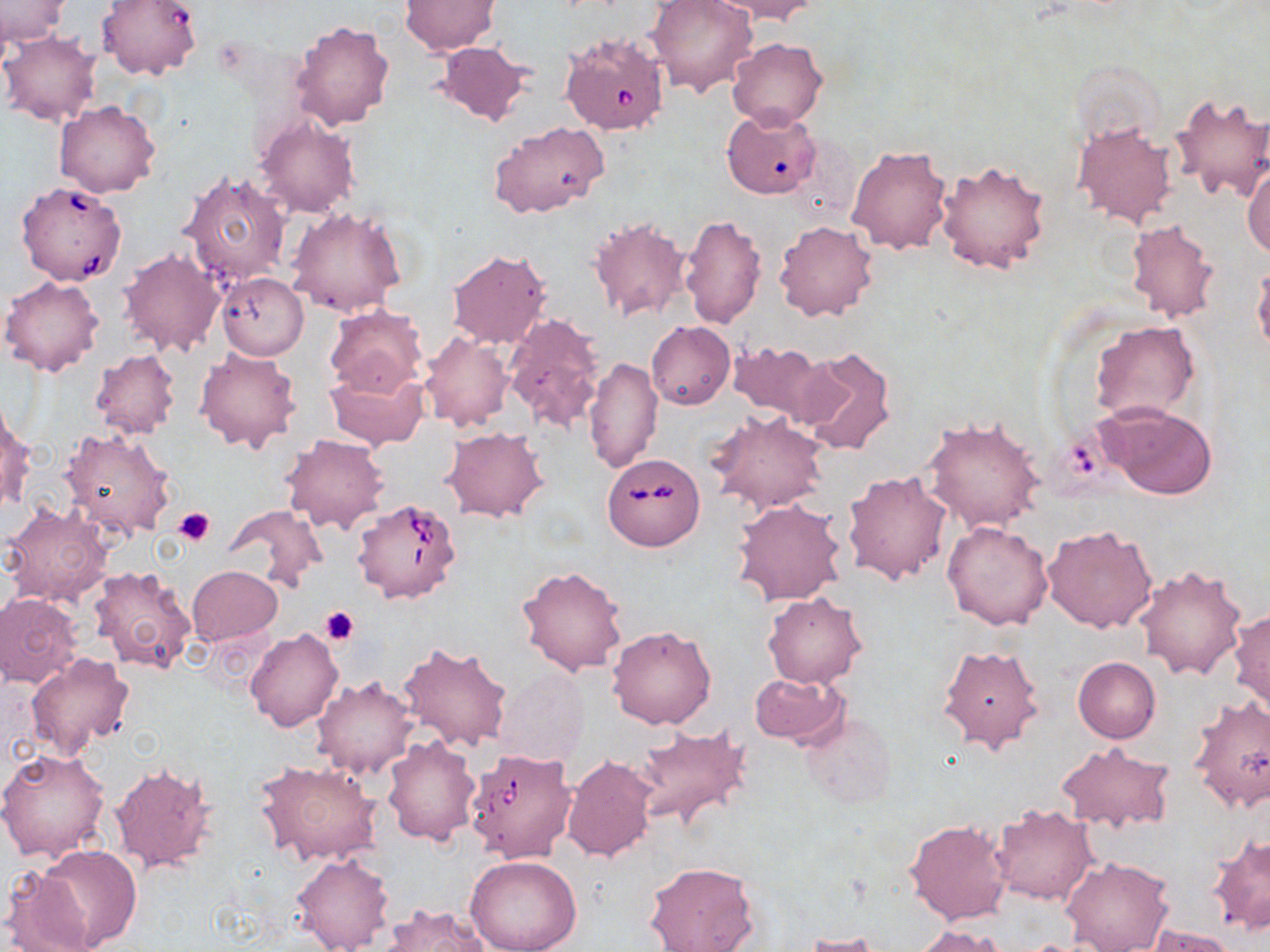

{
  "slide_level_diagnosis": "Babesia divergens",
  "field_of_view": "one of a larger specimen",
  "modality": "light microscopy",
  "magnification": "1000x",
  "stain": "May-Grünwald-Giemsa",
  "platelet_locations": "approximate bounding boxes as (x1, y1, x2, y2) in pixels: (172, 507, 215, 546), (320, 607, 359, 645)",
  "preparation": "thin blood smear",
  "image_size": "1270×952 pixels",
  "babesia_divergens_infected_red_blood_cell_locations": "approximate bounding boxes as (x1, y1, x2, y2) in pixels: (560, 32, 670, 136), (15, 180, 128, 286), (603, 451, 704, 551), (351, 497, 462, 603), (465, 749, 578, 862)",
  "uninfected_red_blood_cell_locations": "approximate bounding boxes as (x1, y1, x2, y2) in pixels: (1, 0, 68, 46), (98, 0, 202, 80), (646, 0, 759, 97), (713, 0, 820, 23), (2, 1, 83, 87), (399, 1, 500, 55), (290, 19, 394, 129), (0, 31, 101, 125), (727, 37, 826, 129), (431, 39, 532, 126), (1170, 92, 1270, 204), (56, 101, 160, 198), (723, 108, 821, 199), (253, 113, 362, 218), (488, 120, 609, 220), (1072, 122, 1178, 229), (847, 145, 951, 254), (936, 158, 1049, 275), (1244, 163, 1270, 260), (179, 169, 291, 289), (286, 206, 405, 318), (680, 214, 765, 331), (588, 216, 691, 323), (1125, 219, 1220, 324), (774, 220, 878, 322), (118, 246, 226, 357), (446, 249, 552, 348), (1252, 262, 1270, 358), (217, 273, 308, 359), (1, 276, 104, 377), (324, 306, 427, 398), (503, 313, 605, 436), (646, 320, 735, 409), (1090, 322, 1199, 424), (419, 331, 514, 432), (726, 339, 831, 425), (89, 348, 182, 439), (195, 348, 303, 453), (797, 348, 898, 456), (584, 358, 662, 472), (324, 368, 428, 452), (1095, 401, 1216, 500), (1, 405, 32, 517), (707, 411, 827, 513), (921, 417, 1046, 534), (441, 427, 549, 522), (60, 428, 176, 540), (281, 433, 390, 534), (842, 471, 952, 586), (732, 498, 846, 606), (2, 503, 113, 605), (224, 504, 326, 594), (942, 519, 1053, 630), (1042, 524, 1158, 633), (1134, 564, 1247, 682), (88, 565, 197, 673), (187, 565, 282, 646), (516, 565, 628, 677), (763, 592, 866, 688), (0, 593, 83, 687), (1230, 607, 1270, 717), (607, 625, 717, 730), (246, 627, 342, 731), (397, 639, 512, 751), (937, 642, 1045, 753), (27, 653, 135, 761), (1072, 657, 1160, 744), (496, 671, 589, 765), (749, 671, 849, 748), (312, 676, 420, 779), (761, 678, 884, 796), (1187, 694, 1270, 812), (799, 708, 898, 808), (633, 722, 752, 832), (382, 734, 481, 844), (1055, 741, 1176, 833), (0, 746, 110, 862), (561, 755, 657, 861), (255, 759, 382, 865), (108, 763, 219, 877), (990, 804, 1096, 904), (904, 819, 1011, 925), (1208, 833, 1270, 935), (32, 845, 142, 950), (291, 852, 394, 952), (466, 854, 583, 952), (1060, 855, 1175, 952), (644, 861, 758, 951), (3, 866, 99, 952), (379, 904, 490, 952), (912, 926, 1009, 951), (1147, 926, 1237, 952), (801, 933, 891, 952)"
}